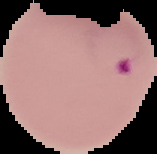
preparation: thin blood film
malaria_status: parasitized
image_size: 157×154 pixels
image_type: cell region segmented out of the field of view; surrounding area masked to black